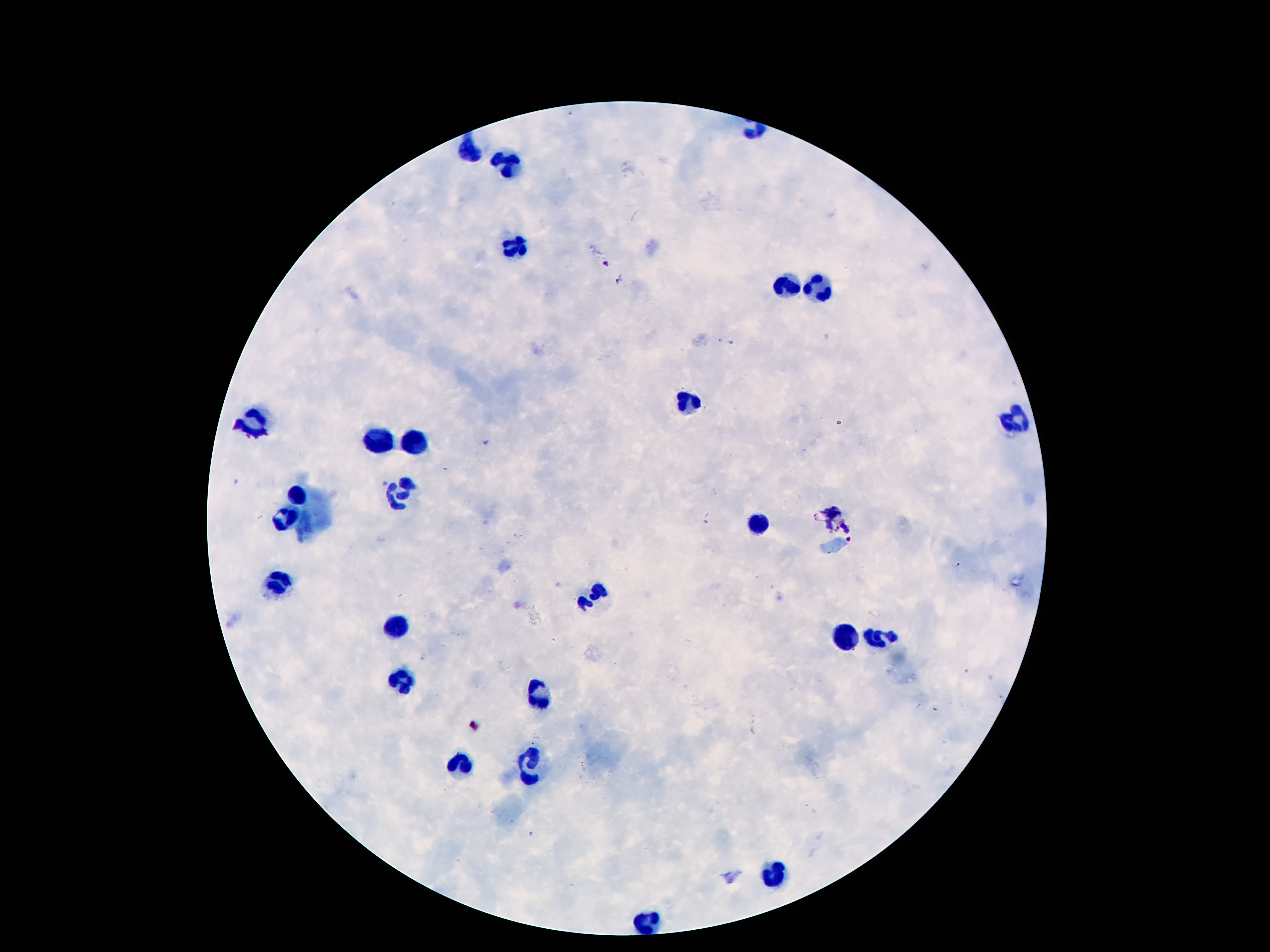
Approximate centers as {x, y} in pixels. Leukocyte locations: {466, 153}, {508, 161}, {517, 247}, {786, 288}, {821, 289}, {688, 402}, {1016, 418}, {245, 421}, {416, 439}, {379, 440}, {401, 496}, {298, 497}, {286, 518}, {758, 522}, {277, 585}, {595, 595}, {399, 629}, {847, 638}, {879, 639}, {404, 680}, {537, 693}, {463, 762}, {531, 763}, {773, 873}, {651, 922}. 100x magnification. Patient malaria status: negative. Thick blood smear. One field from this slide. Smartphone photograph taken through the microscope eyepiece. Image is 1270×952 pixels. Giemsa-stained preparation.